State which parasite is depicted.
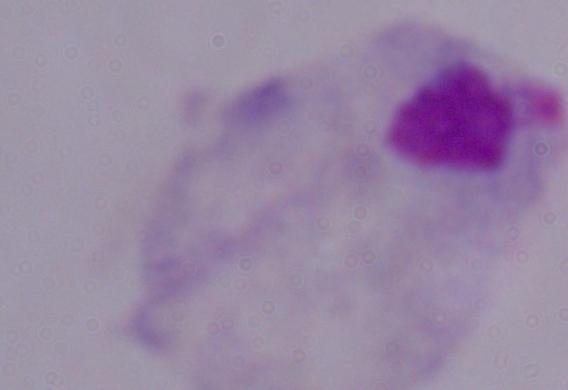

This is a trichomonad.

{
  "magnification": "1000x",
  "modality": "micrograph"
}